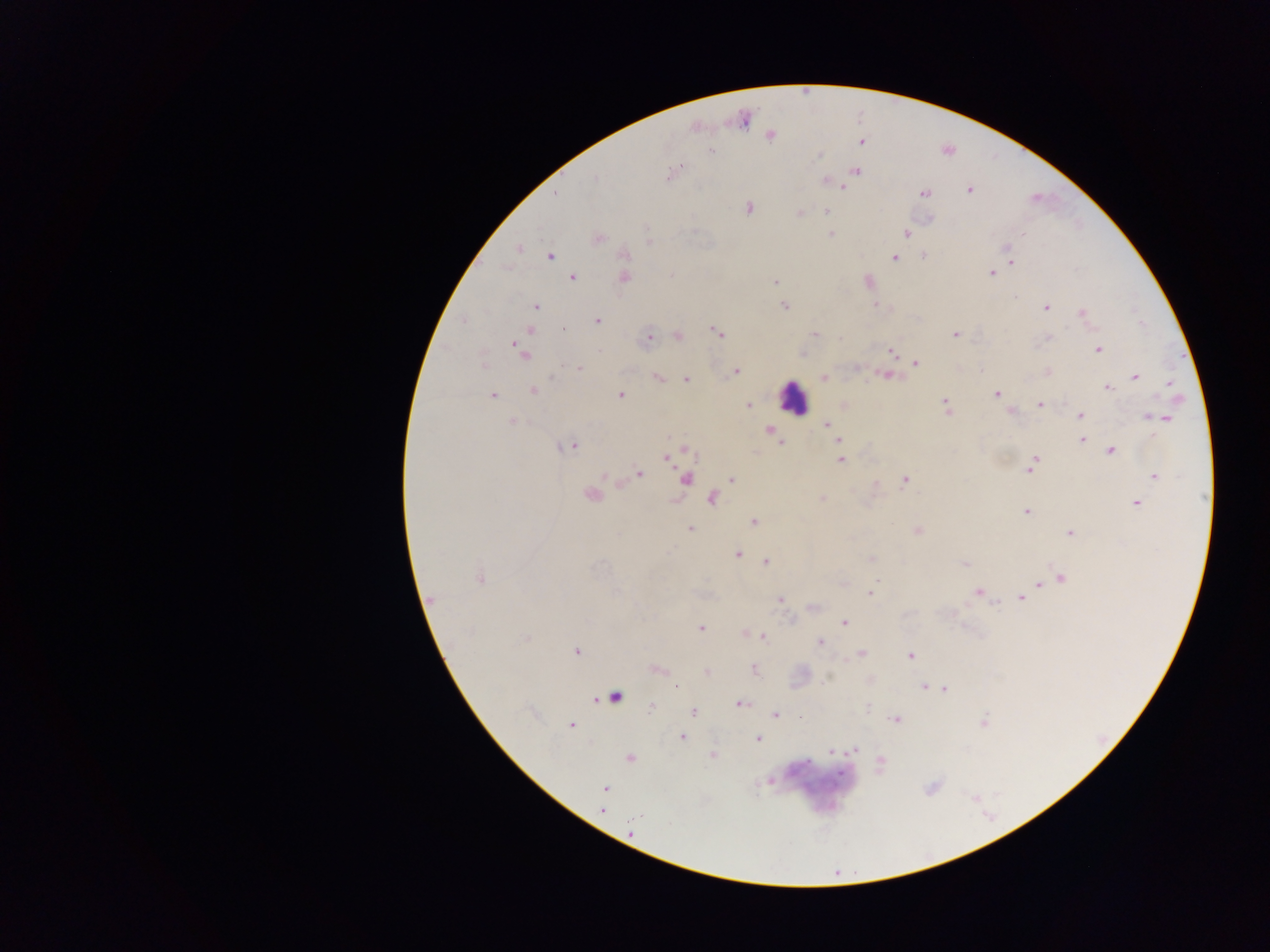
Approximate centers as x y in pixels. Malaria parasite locations: 742 119; 770 134; 861 141; 710 152; 855 171; 672 173; 826 181; 843 186; 969 190; 923 192; 748 208; 826 211; 799 213; 930 218; 830 233; 906 233; 597 238; 648 241; 1005 247; 518 248; 549 255; 623 255; 923 255; 894 258; 1011 263; 992 273; 671 274; 571 277; 623 277; 867 280; 773 281; 878 305; 535 306; 784 306; 1046 307; 1082 313; 597 321; 531 330; 717 333; 814 334; 955 334; 678 336; 647 338; 1047 338; 1098 349; 519 350; 892 351; 803 353; 916 362; 579 368; 735 371; 1047 372; 887 375; 1134 376; 656 377; 824 377; 686 379; 1170 383; 1107 387; 533 391; 492 394; 621 394; 995 394; 1039 404; 748 405; 844 405; 945 405; 1012 411; 1080 415; 1150 415; 1164 417; 512 421; 826 423; 770 430; 774 438; 838 440; 1081 440; 780 442; 570 447; 686 447; 1110 450; 665 456; 839 459; 1035 461; 1030 469; 638 473; 1156 476; 684 478; 731 479; 904 479; 590 496; 712 498; 822 498; 1136 503; 1026 511; 753 521; 691 528; 916 530; 1070 533; 737 554; 870 558; 765 560; 965 564; 1061 577; 480 578; 1040 583; 979 592; 871 593; 1020 598; 779 599; 430 601; 813 607; 844 621; 700 628; 742 632; 763 636; 819 641; 576 651; 861 653; 910 654; 753 668; 658 669; 707 672; 923 686; 929 688; 943 689; 613 697; 739 704; 652 705; 693 712; 774 715; 896 719; 983 722; 572 724; 682 737; 757 739; 854 750; 830 751; 713 755; 629 758; 879 762; 770 782; 605 788; 602 810; 630 832. Leukocyte locations: 792 397; 815 785. Single field of view. Image is 1270×952 pixels. Sample from Ghana. Thick blood smear. Photographed through a microscope with a mobile-phone camera.